Look for Plasmodium parasites.
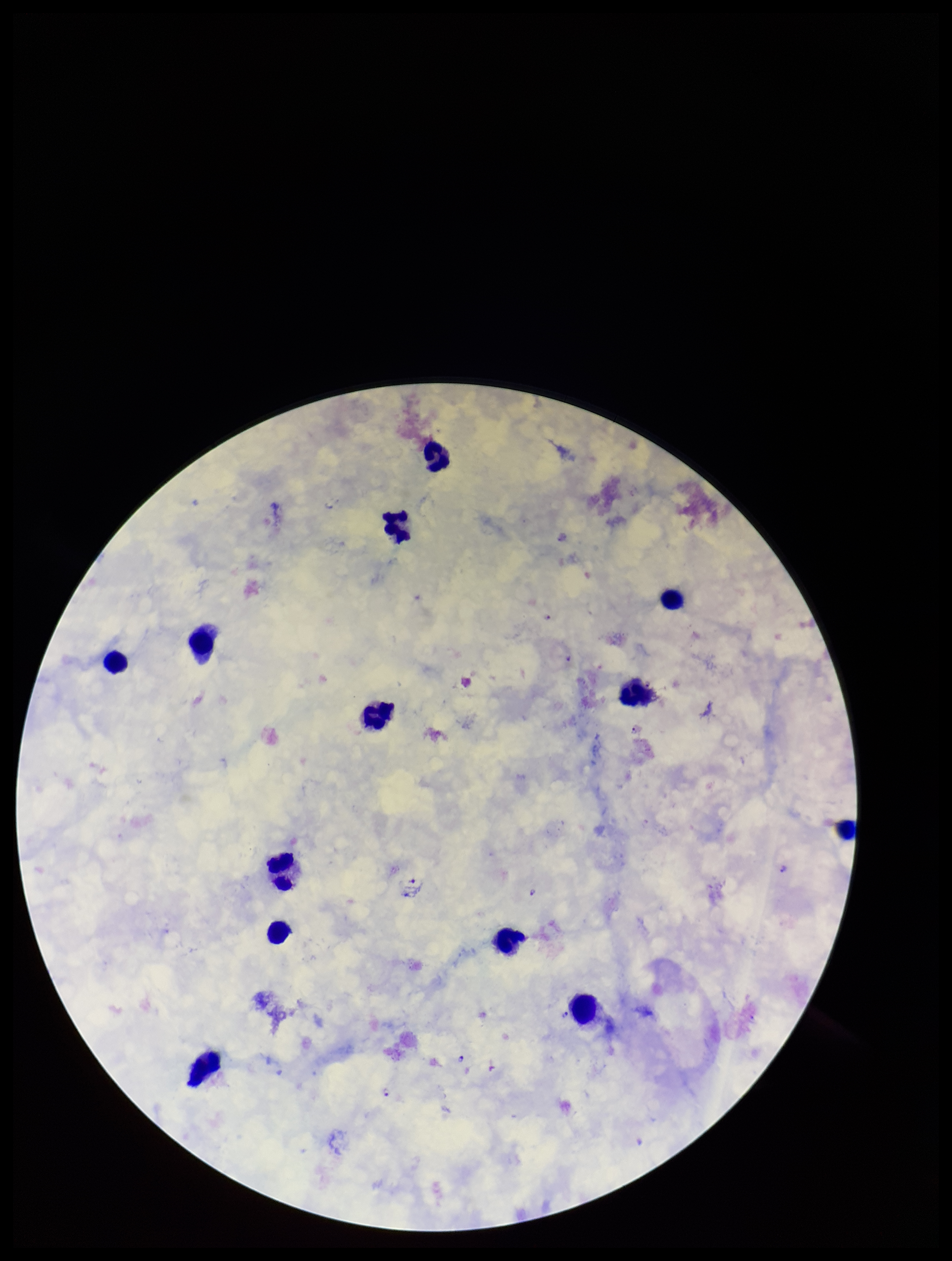

Seen.

parasite count = 8
capture = smartphone photograph through the microscope eyepiece
leukocyte count = 13
image size = 952×1261 pixels
stain = Giemsa
species reported for this patient = Plasmodium falciparum
preparation = thick
patient malaria status = infected
field of view = one from this slide